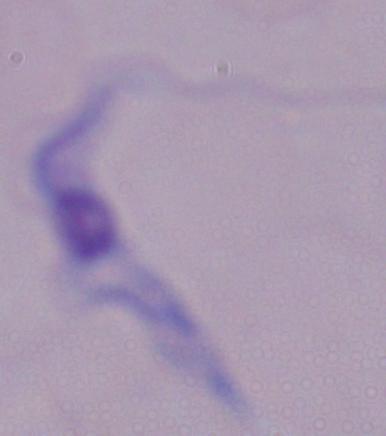

magnification: 1000x
modality: photomicrograph
identification: trypanosome